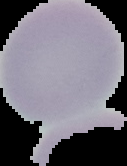
{
  "image_size": "127×166 pixels",
  "result": "no Plasmodium parasites detected",
  "image_type": "segmented cell region with the area outside set to black",
  "preparation": "thin blood smear"
}